Identify the blood parasite species.
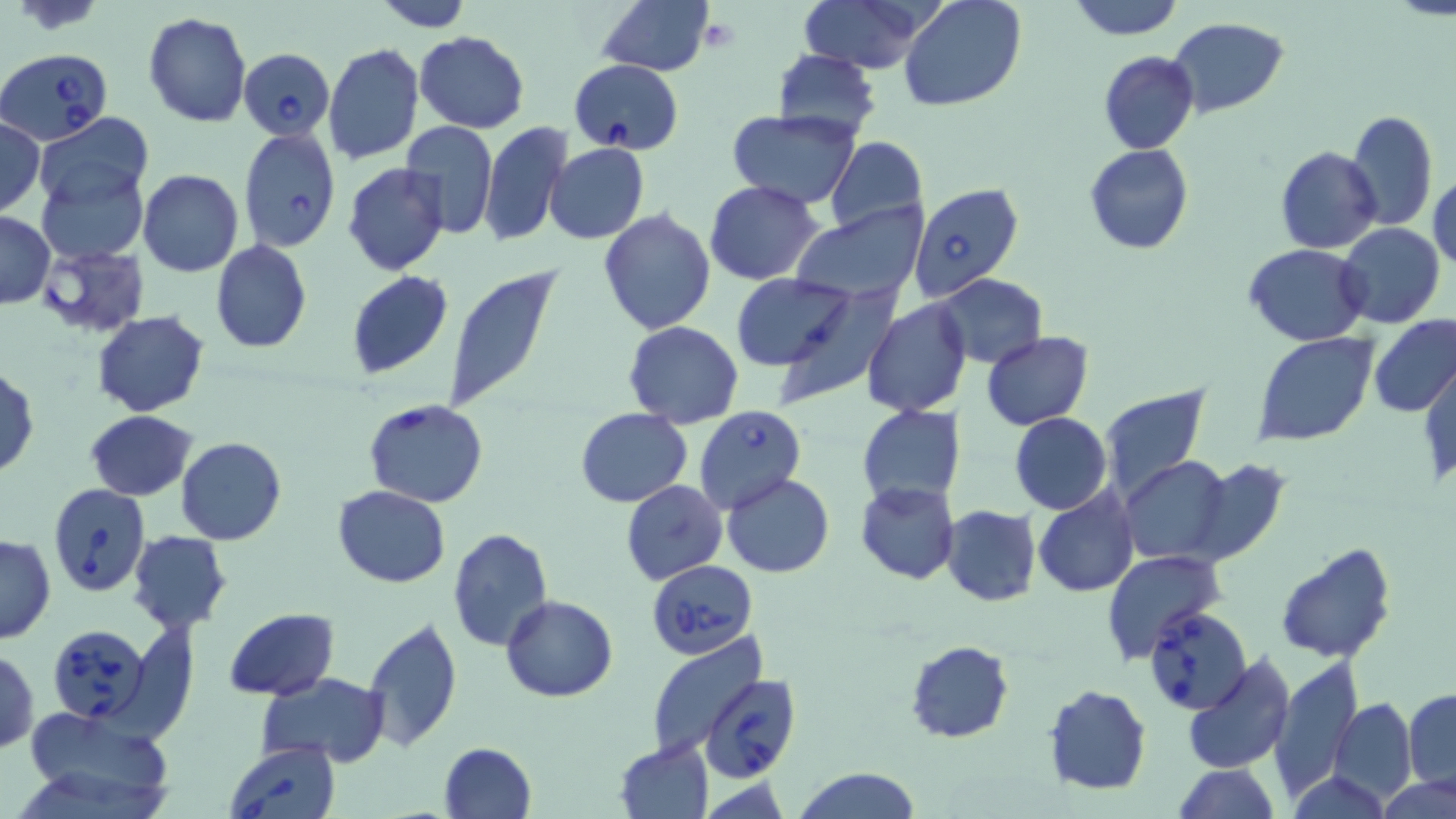

Babesia divergens.

Approximate bounding boxes as (x1,y1)-(x2,y2) corner pairs in pixels. Uninfected red blood cell locations: (369,0)-(473,31), (596,0)-(714,76), (800,0)-(932,74), (901,0)-(1025,110), (1066,0)-(1184,39), (142,12)-(251,127), (1168,18)-(1289,118), (415,30)-(530,132), (322,44)-(423,165), (770,49)-(881,140), (1098,51)-(1198,155), (1347,109)-(1438,233), (37,111)-(153,210), (725,112)-(862,208), (0,117)-(44,216), (479,121)-(569,248), (399,122)-(499,239), (824,137)-(928,237), (546,142)-(649,243), (1084,143)-(1194,254), (1275,146)-(1381,254), (343,163)-(449,277), (37,166)-(147,263), (138,169)-(243,277), (1429,172)-(1456,274), (705,180)-(825,285), (789,203)-(928,307), (598,207)-(716,334), (0,210)-(55,307), (1336,222)-(1445,329), (211,241)-(311,353), (1244,243)-(1368,347), (442,263)-(562,415), (347,270)-(453,379), (935,273)-(1047,368), (731,274)-(857,370), (768,286)-(900,411), (862,300)-(970,418), (94,312)-(210,416), (1368,314)-(1456,419), (625,321)-(743,428), (981,331)-(1094,430), (1252,332)-(1378,448), (1421,362)-(1455,486), (1,366)-(39,478), (1098,387)-(1211,505), (858,404)-(967,506), (575,408)-(692,507), (84,410)-(198,500), (1009,411)-(1111,513), (176,436)-(287,546), (1119,457)-(1234,564), (1190,460)-(1291,566), (722,472)-(834,578), (620,480)-(728,586), (855,481)-(960,584), (333,485)-(450,588), (1033,487)-(1139,597), (940,505)-(1042,606), (447,527)-(553,651), (129,531)-(231,635), (0,533)-(55,643), (1274,542)-(1397,665), (1102,548)-(1225,665), (500,595)-(619,702), (225,607)-(339,701), (359,617)-(463,753), (645,634)-(768,756), (904,640)-(1014,744), (1,648)-(40,755), (1181,652)-(1296,774), (1270,656)-(1363,799), (257,672)-(391,764), (1043,684)-(1151,795), (1404,689)-(1456,794), (1330,698)-(1416,804), (20,705)-(174,814), (614,738)-(714,819), (439,741)-(536,819), (1167,763)-(1281,819), (792,767)-(921,819), (1286,769)-(1391,818), (1378,773)-(1456,819). Platelet locations: (696,14)-(743,56). Babesia divergens-infected red blood cell locations: (2,48)-(115,144), (240,48)-(335,140), (568,58)-(683,153), (238,126)-(341,252), (910,182)-(1024,302), (34,244)-(151,338), (363,398)-(489,508), (695,405)-(808,516), (48,484)-(150,597), (646,558)-(759,657), (1143,604)-(1251,714), (46,622)-(153,726), (699,674)-(801,784), (224,741)-(341,819). Image is 1456×819 pixels. Thin blood smear. One field of a larger specimen. Captured at 1000x magnification. May-Grünwald-Giemsa stain. Optical microscopy.